State which parasite is depicted.
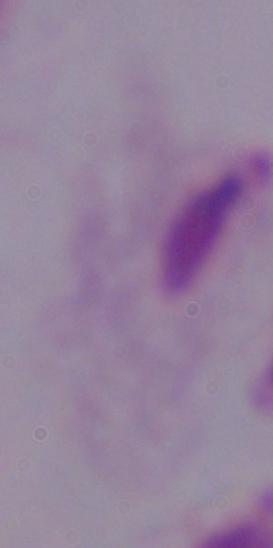

A trichomonad.

1000x magnification. Micrograph.